Point out each Plasmodium parasite.
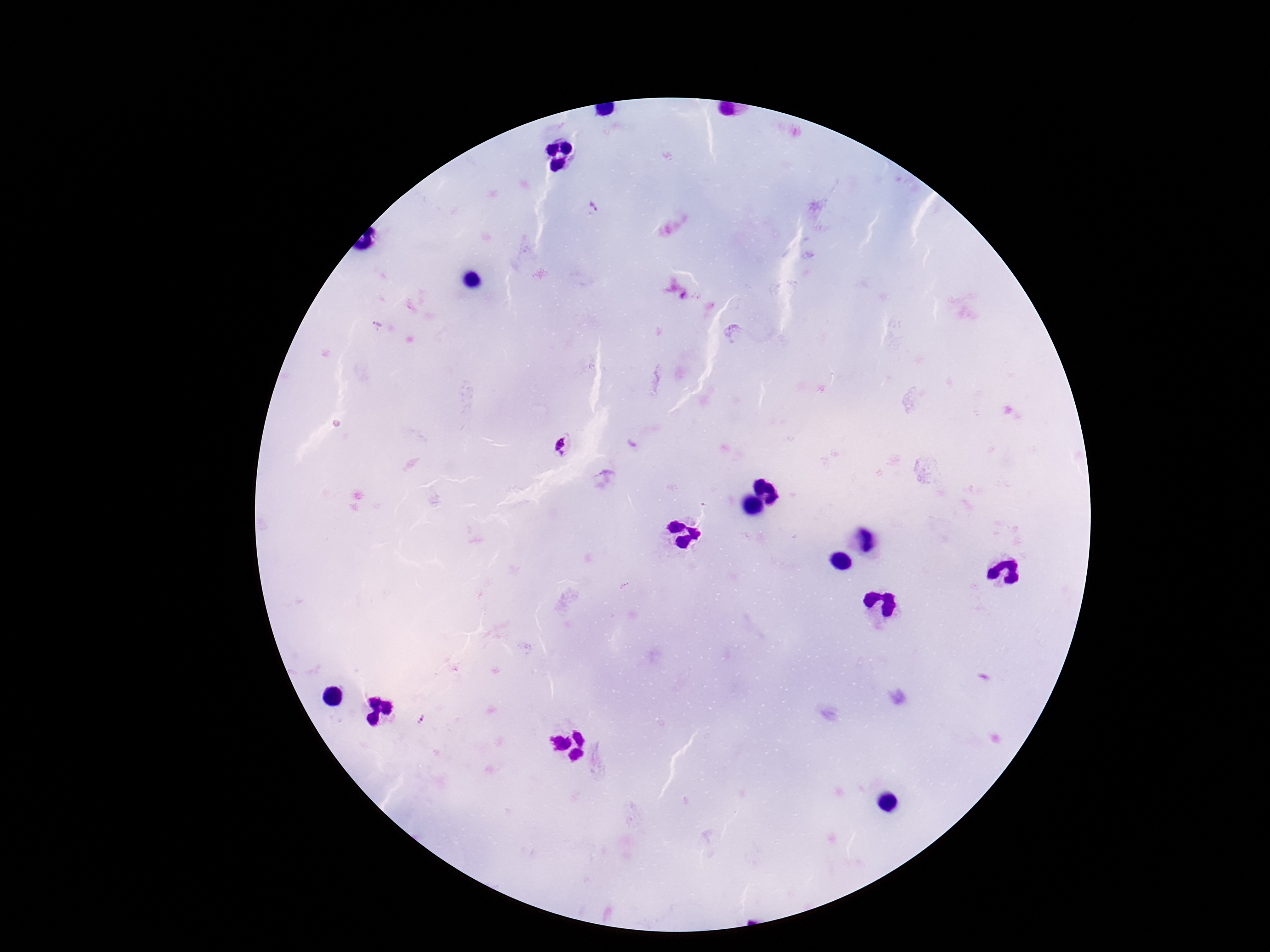

Approximate object centers, in pixels from the top-left corner.
Plasmodium parasites: (x=591, y=209), (x=378, y=325), (x=564, y=447), (x=420, y=719).

{
  "preparation": "thick blood smear",
  "field_of_view": "single",
  "stain": "Giemsa",
  "magnification": "100x",
  "image_size": "1270×952 pixels",
  "patient_malaria_status": "positive",
  "capture": "smartphone camera through the microscope eyepiece"
}